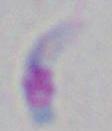

Summary:
  - Magnification: 1000x
  - Modality: micrograph
  - Identification: Toxoplasma gondii